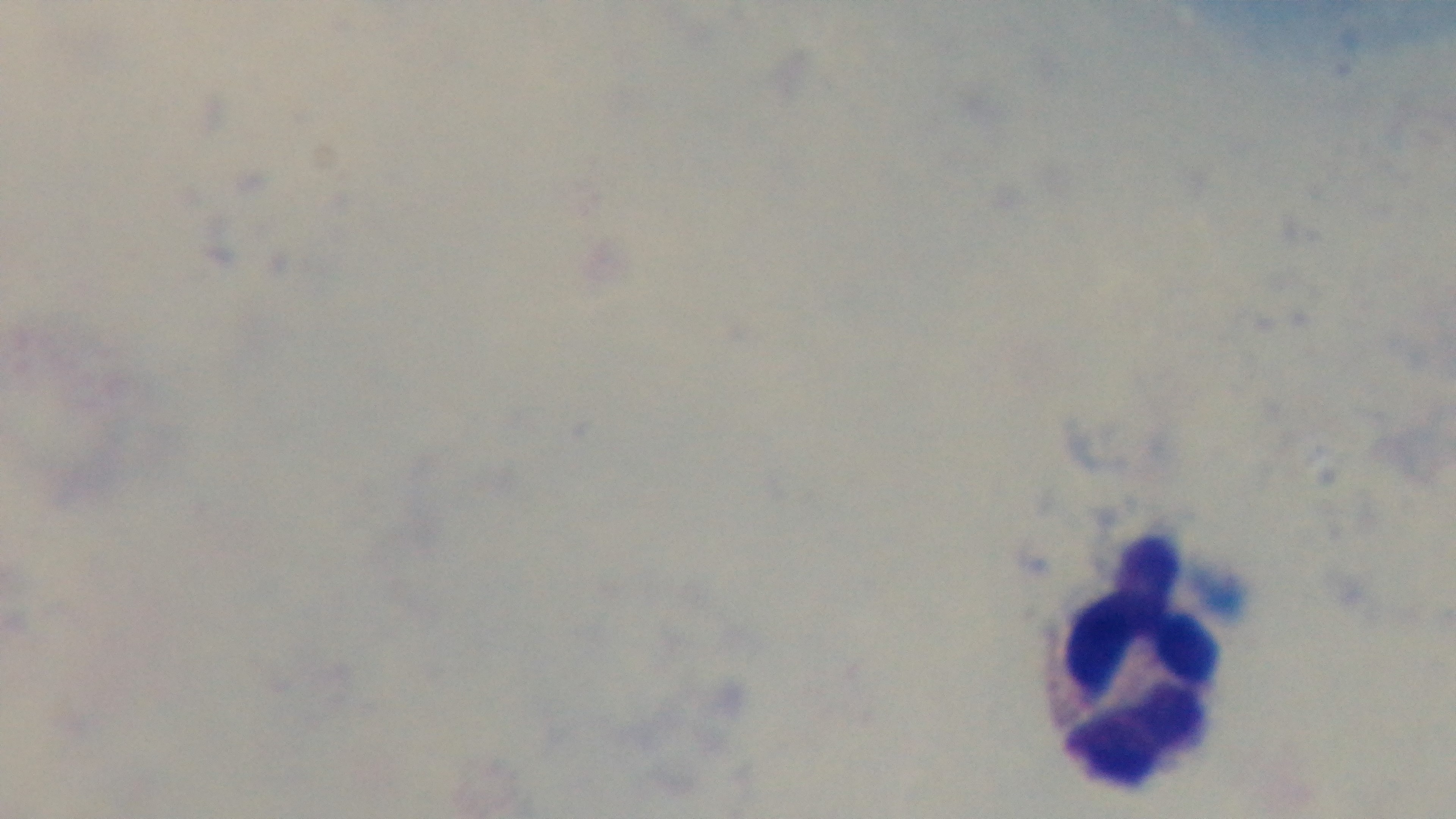
objective = 100x oil immersion
capture = mounted 4K digital camera
malaria status = uninfected
modality = light microscopy
stain = Giemsa
field of view = one from the slide
preparation = thick smear